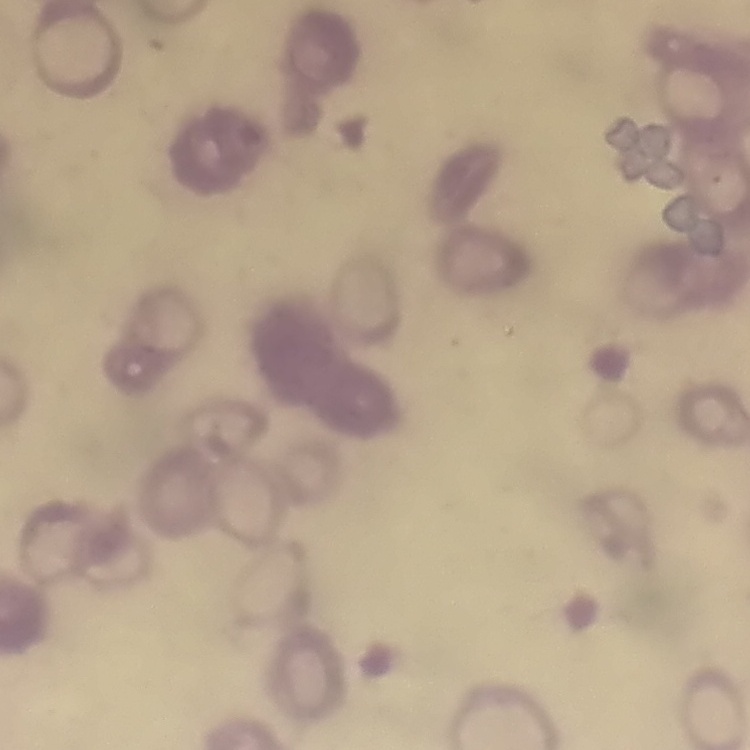
erythrocyte morphology = rouleaux formation
image type = square crop of a larger photomicrograph
stain = Field's or Giemsa
preparation = thin blood film